Outline each blood parasite and name the species.
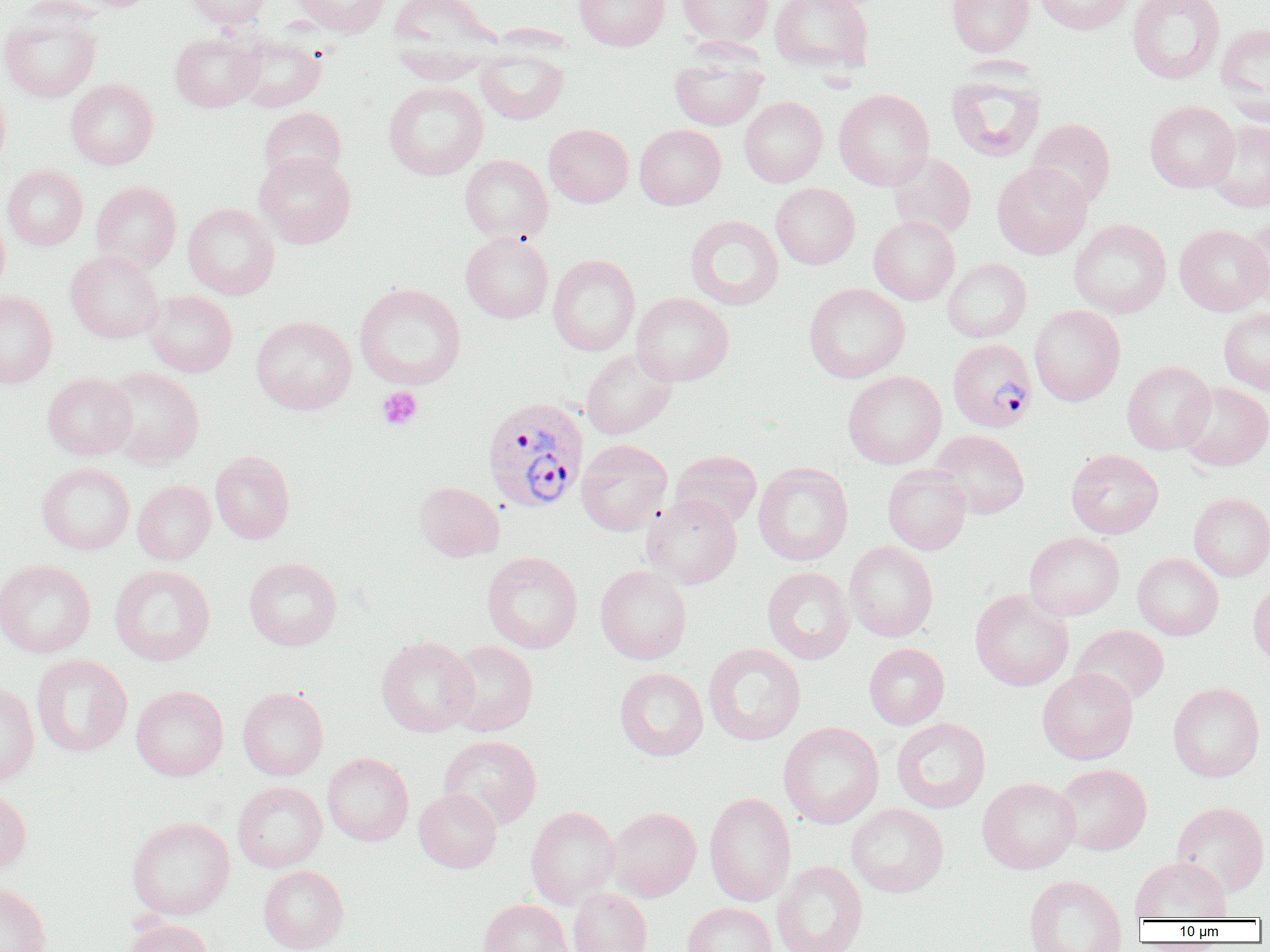

Approximate bounding boxes as [x1, y1, x2, y2] in pixels.
Plasmodium vivax-infected red blood cells: [948, 338, 1037, 432], [482, 397, 588, 513].
No Plasmodium falciparum, Plasmodium ovale, Plasmodium malariae, Babesia divergens, or Trypanosoma brucei observed.

Summary:
  - Uninfected red blood cell locations: [184, 0, 273, 28], [288, 0, 393, 37], [388, 0, 502, 82], [575, 0, 670, 50], [677, 0, 773, 47], [769, 0, 873, 73], [946, 0, 1035, 57], [1035, 0, 1133, 34], [1127, 0, 1225, 83], [1, 5, 102, 103], [1216, 22, 1270, 121], [169, 31, 264, 112], [233, 33, 326, 111], [475, 45, 569, 125], [669, 47, 768, 131], [945, 68, 1047, 162], [66, 79, 158, 169], [383, 81, 488, 180], [0, 82, 11, 175], [834, 89, 934, 190], [739, 96, 827, 187], [1145, 101, 1239, 192], [259, 107, 346, 184], [1027, 118, 1115, 209], [1205, 119, 1270, 212], [544, 124, 633, 207], [634, 124, 726, 209], [888, 151, 976, 239], [254, 152, 357, 248], [459, 154, 553, 243], [992, 162, 1091, 259], [2, 165, 87, 250], [90, 181, 181, 273], [771, 183, 860, 269], [183, 203, 279, 299], [0, 212, 10, 297], [1239, 213, 1270, 308], [685, 215, 784, 310], [869, 216, 960, 304], [1069, 219, 1171, 318], [1174, 224, 1269, 315], [460, 232, 553, 323], [65, 251, 164, 343], [547, 254, 640, 356], [942, 258, 1031, 342], [354, 283, 466, 389], [804, 283, 910, 383], [0, 291, 58, 388], [144, 291, 237, 377], [631, 293, 733, 386], [1029, 305, 1125, 406], [1219, 308, 1270, 395], [250, 316, 356, 414], [581, 349, 677, 439], [1122, 361, 1216, 454], [103, 367, 204, 469], [843, 371, 946, 469], [43, 373, 136, 460], [1178, 382, 1270, 471], [931, 430, 1029, 519], [576, 439, 672, 536], [1066, 449, 1163, 538], [210, 450, 294, 544], [670, 450, 762, 530], [753, 462, 853, 566], [37, 463, 134, 554], [883, 464, 971, 554], [133, 480, 215, 564], [414, 481, 505, 562], [1189, 492, 1270, 581], [641, 494, 742, 589], [1024, 532, 1124, 620], [844, 541, 938, 642], [482, 551, 583, 653], [1133, 553, 1223, 640], [244, 558, 342, 650], [0, 559, 96, 658], [109, 564, 216, 666], [595, 565, 692, 664], [762, 567, 855, 664], [1248, 579, 1270, 667], [970, 589, 1074, 691], [1071, 625, 1169, 706], [376, 636, 478, 737], [444, 641, 538, 736], [703, 643, 806, 745], [864, 643, 950, 729], [31, 654, 133, 757], [614, 667, 708, 761], [1037, 668, 1138, 764], [0, 682, 39, 785], [1167, 682, 1265, 782], [131, 685, 229, 780], [237, 687, 328, 780], [891, 717, 991, 813], [778, 721, 884, 829], [439, 735, 542, 830], [322, 752, 414, 846], [1055, 763, 1151, 855], [978, 777, 1080, 874], [232, 781, 326, 872], [0, 785, 32, 873], [414, 789, 501, 872], [704, 792, 796, 907], [1171, 801, 1270, 896], [846, 803, 949, 897], [526, 806, 620, 909], [607, 807, 701, 901], [127, 816, 235, 920], [1130, 856, 1231, 923], [771, 860, 868, 952], [258, 865, 348, 952], [1023, 874, 1126, 952], [0, 882, 51, 952], [567, 887, 652, 952], [479, 898, 571, 952], [682, 902, 776, 952], [120, 918, 214, 952]
  - Platelet locations: [377, 386, 422, 430]
  - Slide-level diagnosis: Plasmodium vivax
  - Modality: light microscopy
  - Field of view: one of a larger specimen
  - Image size: 1270×952 pixels
  - Magnification: 1000x
  - Preparation: thin blood film